Locate every blood parasite and identify its species.
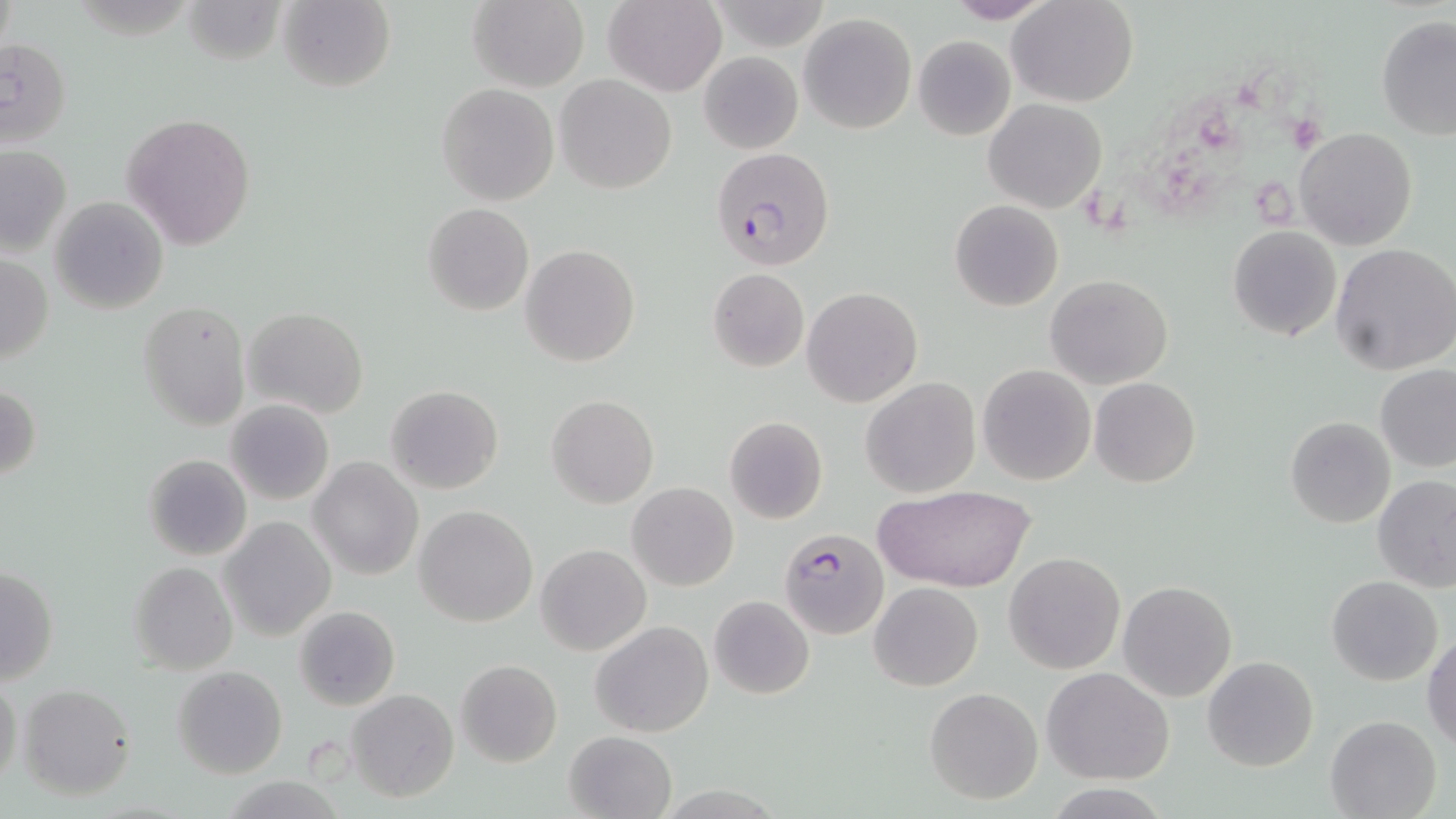
Approximate bounding boxes as (x1, y1, x2, y2) in pixels.
Plasmodium falciparum-infected red blood cells: (709, 146, 835, 269), (778, 526, 889, 639).
No Plasmodium ovale, Plasmodium malariae, Plasmodium vivax, Babesia divergens, or Trypanosoma brucei observed.

Platelet locations: (1245, 63, 1300, 117), (1193, 103, 1245, 154), (1286, 112, 1326, 153), (1160, 143, 1220, 216), (1079, 175, 1137, 240), (1251, 177, 1302, 231). Uninfected red blood cell locations: (179, 0, 285, 65), (279, 0, 396, 92), (466, 0, 588, 90), (603, 0, 728, 97), (941, 0, 1057, 24), (1011, 0, 1138, 107), (799, 13, 917, 134), (1376, 17, 1456, 139), (913, 34, 1017, 141), (1, 37, 72, 148), (698, 51, 803, 154), (555, 74, 676, 193), (436, 83, 559, 205), (983, 98, 1106, 214), (123, 112, 257, 248), (1295, 127, 1418, 250), (0, 145, 72, 257), (50, 196, 170, 314), (949, 199, 1063, 311), (423, 203, 534, 315), (1227, 226, 1343, 343), (520, 243, 639, 366), (1330, 243, 1456, 374), (0, 255, 53, 365), (708, 268, 809, 372), (1046, 274, 1172, 389), (802, 287, 922, 406), (137, 299, 250, 431), (245, 307, 367, 420), (978, 364, 1095, 485), (1374, 364, 1455, 473), (861, 377, 980, 497), (1089, 377, 1201, 487), (1, 384, 42, 483), (386, 384, 504, 493), (546, 393, 660, 508), (226, 400, 334, 504), (725, 415, 829, 523), (1284, 417, 1394, 528), (142, 454, 251, 562), (308, 455, 424, 580), (1373, 473, 1456, 593), (627, 482, 739, 591), (876, 483, 1035, 595), (414, 505, 538, 627), (220, 516, 335, 641), (536, 544, 650, 655), (1004, 552, 1125, 675), (129, 561, 238, 675), (0, 566, 59, 684), (1327, 575, 1444, 686), (1118, 579, 1237, 702), (869, 581, 983, 691), (709, 595, 814, 699), (294, 605, 401, 712), (590, 619, 714, 737), (1424, 632, 1456, 750), (1203, 656, 1318, 772), (455, 660, 562, 768), (173, 666, 287, 779), (1043, 667, 1173, 785), (0, 674, 23, 792), (16, 682, 137, 800), (924, 687, 1043, 805), (347, 689, 459, 803), (1325, 715, 1441, 819), (563, 730, 676, 818). Slide-level diagnosis: Plasmodium falciparum. One field of a larger specimen. Light microscopy. Image is 1456×819 pixels. May-Grünwald-Giemsa stain. Thin blood smear. Captured at 1000x magnification.